Locate every blood parasite and identify its species.
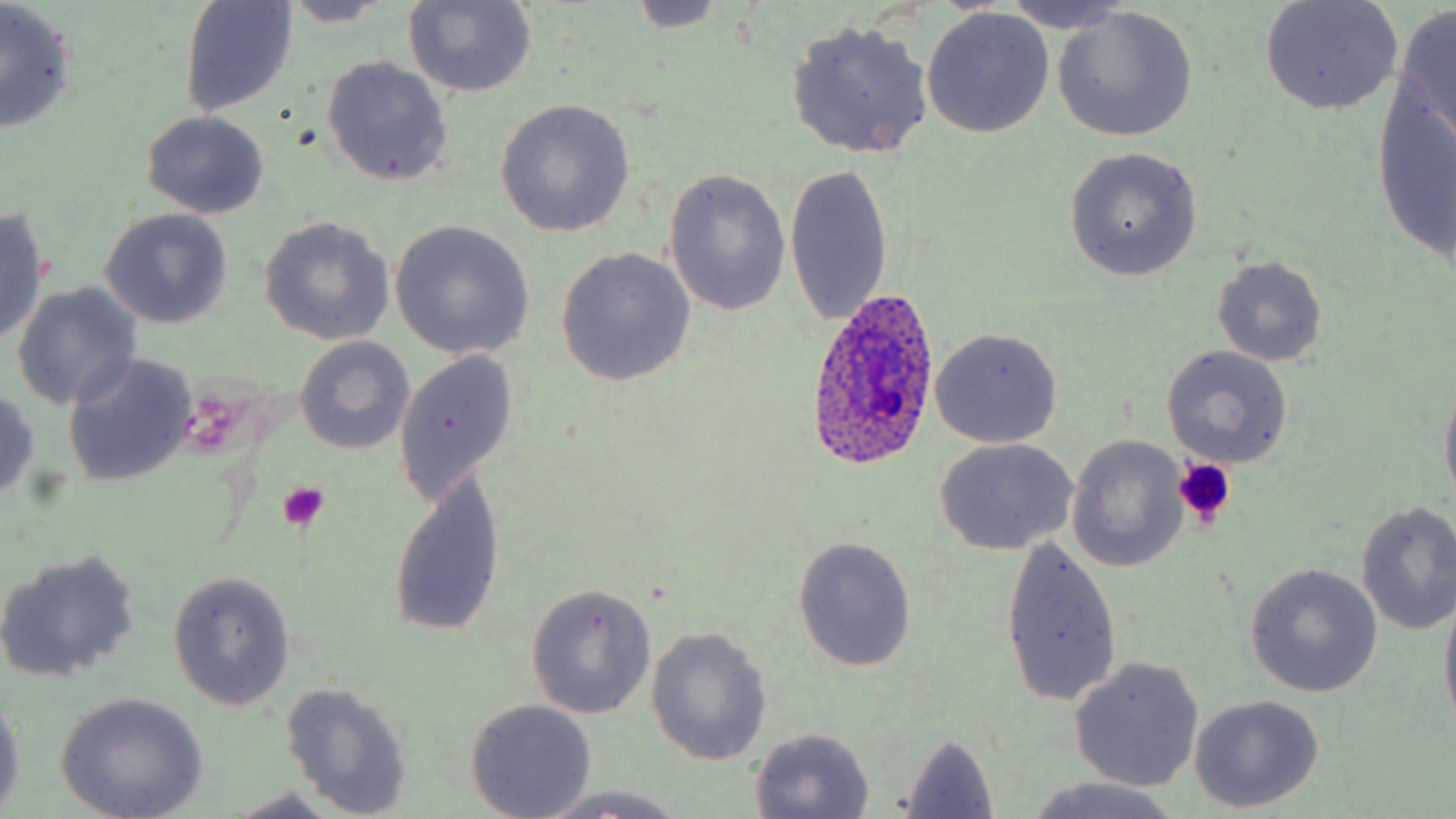
Approximate bounding boxes as (x1,y1)-(x2,y2) corner pairs in pixels.
Plasmodium ovale-infected red blood cells: (806,286)-(942,468).
No Plasmodium falciparum, Plasmodium malariae, Plasmodium vivax, Babesia divergens, or Trypanosoma brucei observed.

slide-level diagnosis = Plasmodium ovale
platelet locations = approximate bounding boxes as (x1,y1)-(x2,y2) corner pairs in pixels: (1173,458)-(1235,529), (278,481)-(329,529)
field of view = one of a larger specimen
uninfected red blood cell locations = approximate bounding boxes as (x1,y1)-(x2,y2) corner pairs in pixels: (179,0)-(300,118), (999,0)-(1138,33), (1258,0)-(1404,116), (402,1)-(536,99), (624,1)-(729,33), (277,2)-(395,27), (0,3)-(78,136), (1391,6)-(1456,149), (1051,7)-(1196,143), (921,8)-(1055,138), (785,19)-(935,160), (321,55)-(454,187), (1372,78)-(1456,269), (497,99)-(635,237), (141,111)-(270,219), (1065,149)-(1202,281), (783,160)-(894,330), (663,167)-(792,318), (0,208)-(51,343), (99,209)-(234,329), (259,217)-(395,345), (389,221)-(536,360), (556,248)-(696,387), (1212,256)-(1326,366), (11,283)-(143,411), (930,327)-(1063,448), (293,336)-(415,455), (1161,345)-(1294,468), (393,349)-(518,506), (63,352)-(198,488), (1438,379)-(1456,511), (0,389)-(42,498), (1066,435)-(1190,572), (935,438)-(1077,555), (385,468)-(507,640), (1354,500)-(1456,636), (794,536)-(917,672), (998,536)-(1122,709), (0,548)-(142,684), (1246,564)-(1383,698), (167,572)-(298,710), (525,584)-(656,719), (1438,585)-(1456,731), (646,627)-(772,765), (1070,657)-(1203,792), (280,680)-(415,817), (0,691)-(24,812), (55,693)-(209,819), (1190,695)-(1324,813), (465,699)-(596,817), (747,727)-(875,817), (897,733)-(1000,819), (1018,778)-(1185,819), (527,786)-(697,819), (225,791)-(357,819)
modality = light microscopy
preparation = thin blood film
magnification = 1000x
stain = May-Grünwald-Giemsa
image size = 1456×819 pixels